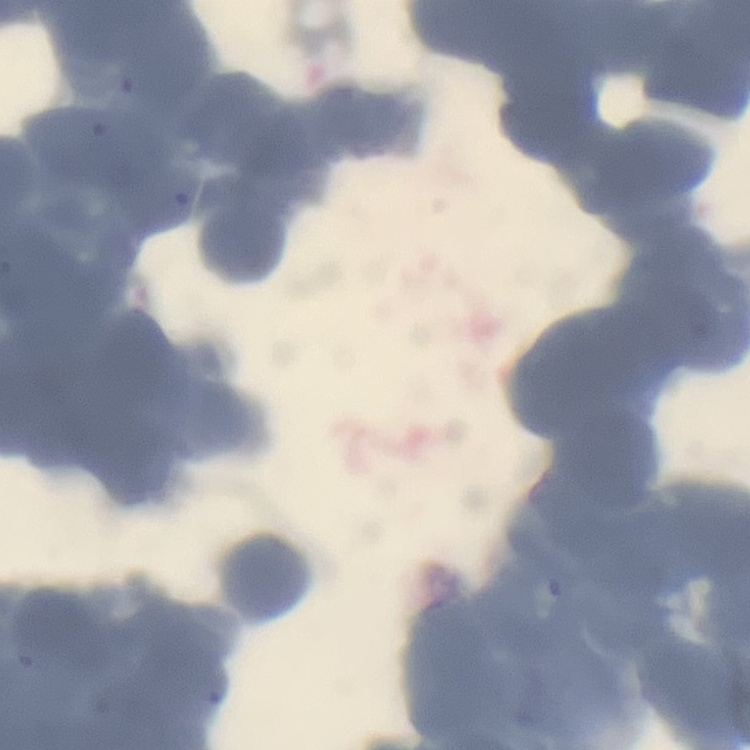
Summary:
  - Red blood cell morphology: rouleaux formation
  - Image type: one tile cut from a larger photomicrograph
  - Preparation: thin blood film
  - Stain: Field's or Giemsa